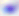
Summary:
  - Magnification: 400x
  - Modality: micrograph
  - Identification: Toxoplasma gondii